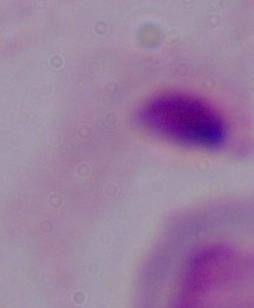

A trichomonad is seen. 1000x magnification. Photomicrograph.